Locate every blood parasite and identify its species.
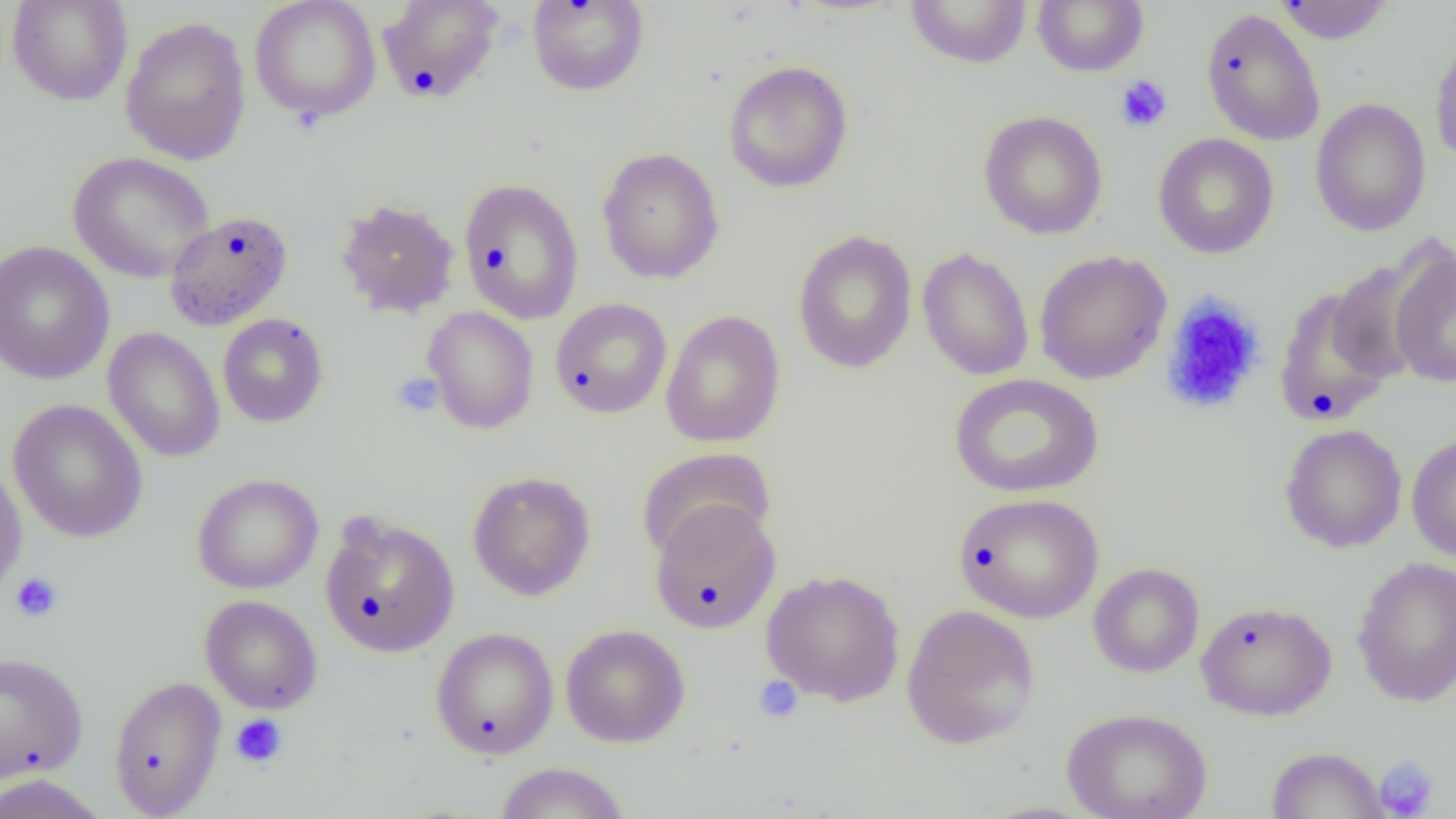

No blood parasites seen.

Approximate bounding boxes as [x1, y1, x2, y2] in pixels. Uninfected red blood cell locations: [6, 0, 133, 106], [249, 0, 382, 122], [376, 0, 504, 104], [904, 0, 1032, 68], [1032, 0, 1149, 76], [526, 1, 649, 96], [1273, 1, 1395, 45], [1200, 7, 1326, 146], [120, 15, 252, 166], [1429, 31, 1456, 167], [723, 60, 854, 194], [1309, 98, 1431, 237], [978, 110, 1108, 240], [1152, 133, 1279, 259], [597, 147, 725, 284], [67, 151, 215, 283], [458, 178, 584, 324], [335, 199, 459, 318], [165, 211, 293, 330], [792, 229, 918, 374], [0, 241, 115, 386], [1388, 245, 1456, 389], [917, 247, 1034, 381], [1033, 250, 1172, 385], [1325, 258, 1440, 385], [1273, 285, 1399, 426], [550, 298, 673, 419], [423, 306, 539, 434], [661, 309, 786, 448], [217, 313, 329, 428], [102, 327, 225, 463], [949, 373, 1104, 498], [7, 398, 148, 543], [1279, 423, 1407, 553], [1406, 434, 1456, 563], [637, 446, 776, 560], [0, 460, 28, 600], [467, 470, 596, 601], [192, 473, 324, 595], [953, 493, 1104, 624], [649, 501, 781, 634], [319, 512, 459, 659], [1351, 556, 1456, 707], [1088, 563, 1205, 678], [761, 569, 905, 706], [199, 595, 323, 714], [1196, 600, 1337, 721], [901, 604, 1040, 750], [560, 624, 690, 748], [430, 627, 559, 759], [0, 651, 89, 783], [108, 675, 227, 817], [1061, 707, 1213, 819], [1265, 746, 1390, 818], [494, 762, 630, 819], [0, 773, 111, 818]. Platelet locations: [1115, 74, 1172, 132], [1160, 294, 1267, 415], [391, 373, 444, 417], [10, 572, 64, 623], [753, 676, 804, 724], [230, 713, 287, 769], [1373, 756, 1440, 818]. Slide-level diagnosis: no evidence of blood parasites. Single field of view. Thin blood smear. Optical microscopy. Captured at 1000x magnification. Image is 1456×819 pixels.